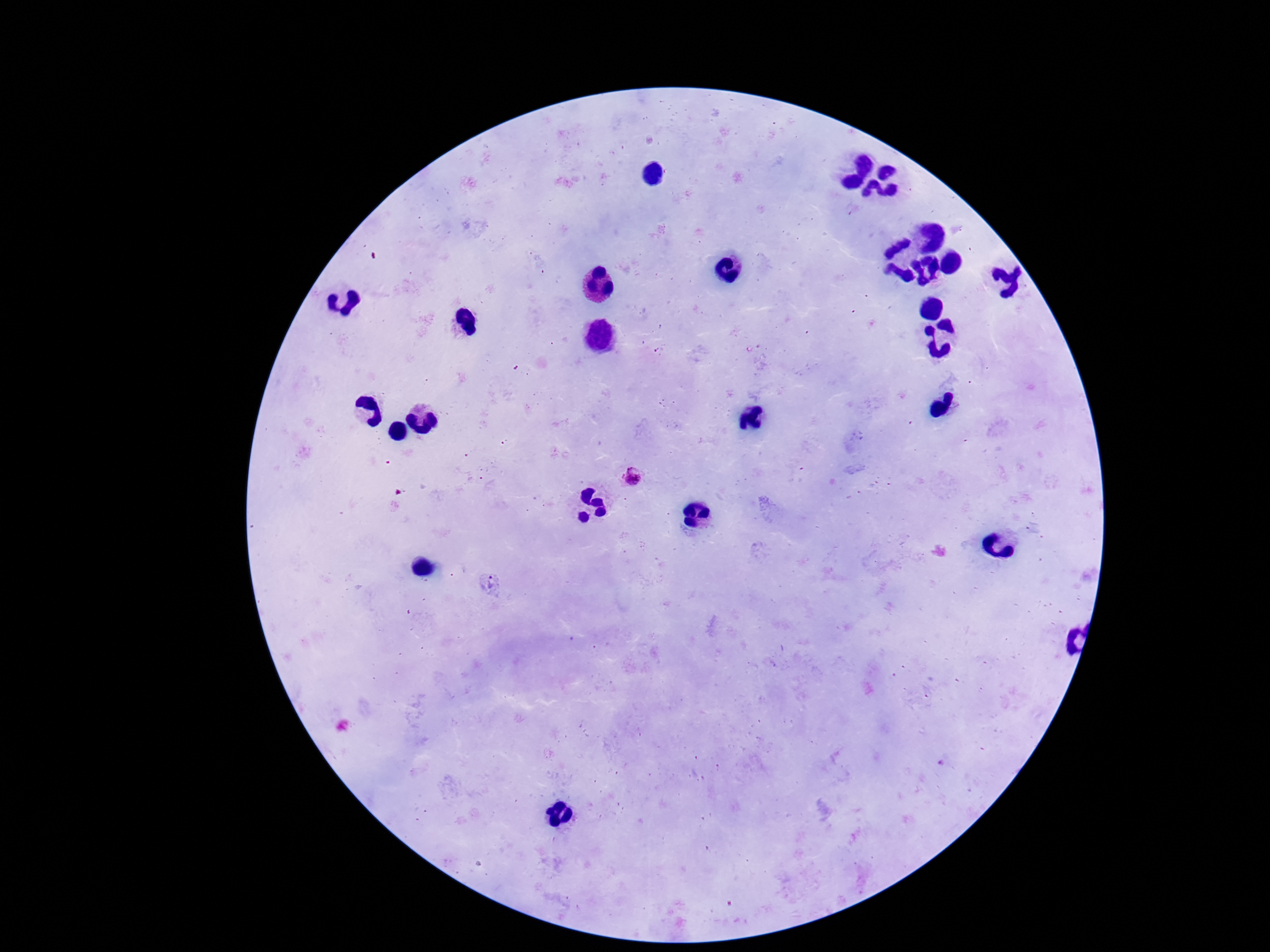 Approximate centers as [x, y] in pixels. Plasmodium parasite locations: [633, 475], [491, 585]. Giemsa-stained preparation. Patient malaria status: positive. Smartphone photograph taken through the microscope eyepiece. One field from this slide. 100x magnification. Image is 1270×952 pixels. Thick blood smear.